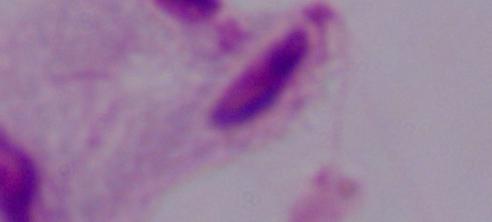

modality = photomicrograph
identification = trichomonad
magnification = 1000x